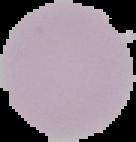

image type = cell region segmented out of the field of view; surrounding area masked to black
result = no malaria parasites seen
image size = 136×142 pixels
preparation = thin blood film